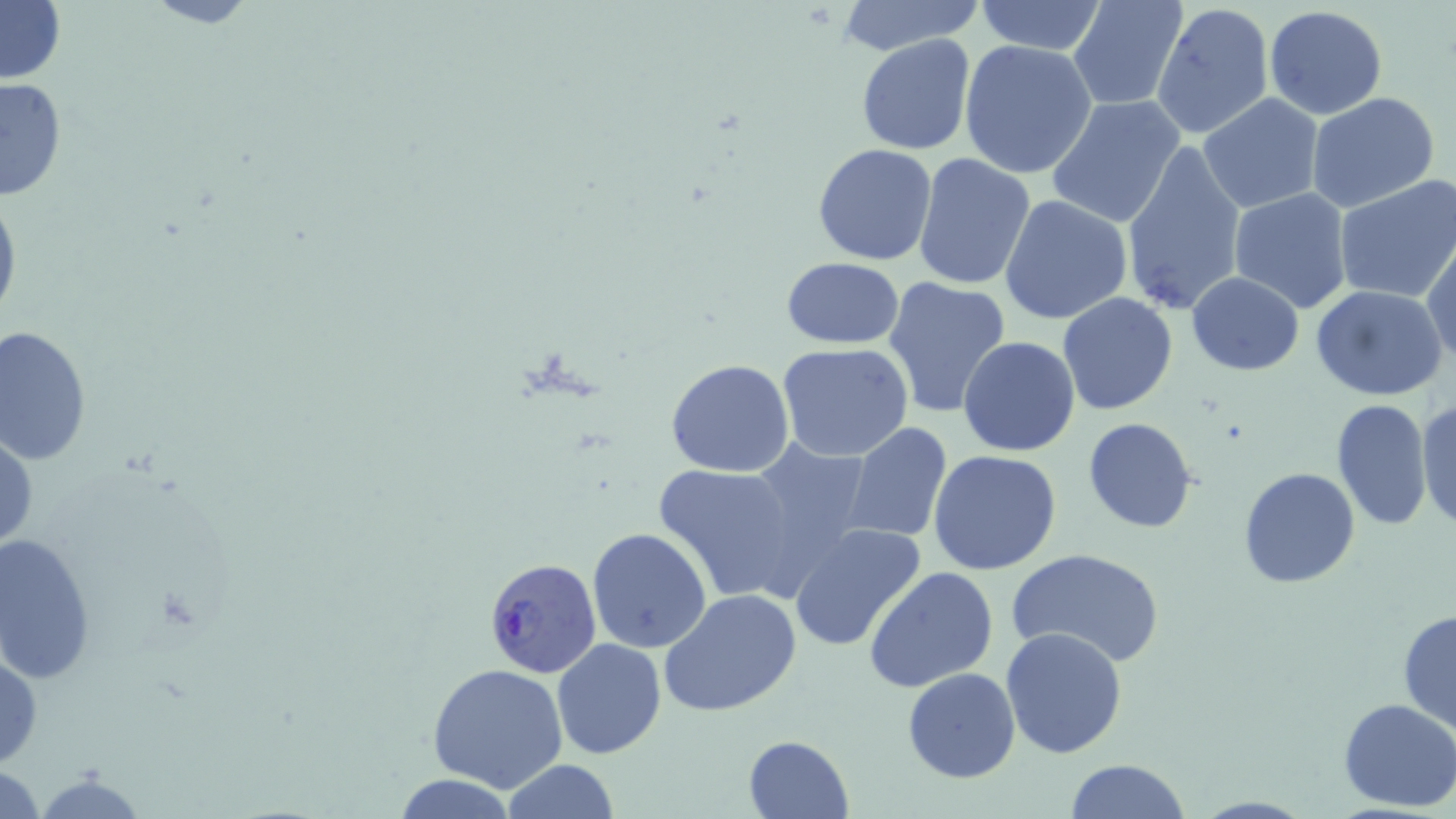

slide-level diagnosis = Plasmodium falciparum
magnification = 1000x
Plasmodium falciparum-infected red blood cell locations = approximate bounding boxes as (x1, y1, x2, y2) in pixels: (481, 557, 601, 679)
uninfected red blood cell locations = approximate bounding boxes as (x1, y1, x2, y2) in pixels: (139, 0, 264, 29), (974, 0, 1109, 55), (1067, 0, 1188, 112), (0, 1, 66, 86), (832, 1, 985, 56), (1150, 1, 1274, 144), (1264, 5, 1388, 120), (855, 34, 978, 156), (1274, 35, 1401, 181), (958, 39, 1097, 178), (0, 76, 69, 203), (1306, 91, 1440, 212), (1198, 94, 1325, 213), (1047, 96, 1186, 228), (1120, 138, 1249, 320), (812, 143, 938, 266), (912, 152, 1035, 290), (1333, 176, 1456, 304), (0, 180, 21, 336), (1228, 189, 1355, 314), (1000, 193, 1133, 325), (1423, 235, 1456, 369), (779, 256, 906, 349), (1187, 273, 1304, 375), (881, 275, 1013, 420), (1310, 285, 1450, 402), (1058, 293, 1179, 414), (0, 325, 92, 467), (958, 336, 1081, 457), (777, 343, 914, 460), (665, 359, 795, 477), (1331, 397, 1434, 532), (1417, 398, 1456, 531), (1083, 417, 1200, 532), (843, 422, 953, 544), (1, 426, 38, 559), (744, 438, 879, 576), (928, 449, 1063, 575), (652, 460, 806, 602), (1237, 466, 1359, 588), (788, 523, 927, 652), (587, 527, 712, 652), (0, 531, 98, 683), (1006, 548, 1166, 669), (864, 565, 998, 692), (660, 589, 804, 718), (1397, 608, 1456, 734), (1001, 626, 1128, 758), (551, 637, 667, 759), (0, 648, 42, 770), (428, 662, 567, 792), (902, 668, 1020, 783), (1337, 699, 1456, 812), (742, 734, 856, 819), (502, 759, 619, 818), (1065, 759, 1191, 819), (0, 761, 47, 817), (31, 769, 151, 819), (391, 774, 522, 817)
field of view = one of a larger specimen
stain = May-Grünwald-Giemsa
modality = light microscopy
preparation = thin blood film
image size = 1456×819 pixels